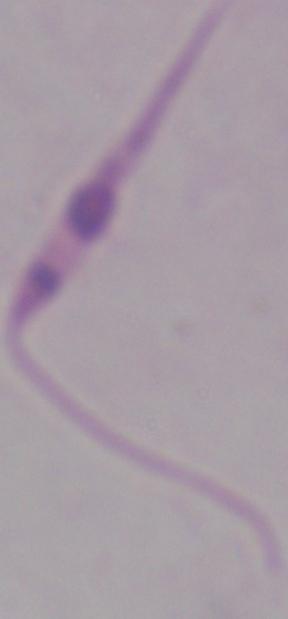
Summary:
  - Magnification: 1000x
  - Identification: Leishmania
  - Modality: micrograph